Name the parasite shown.
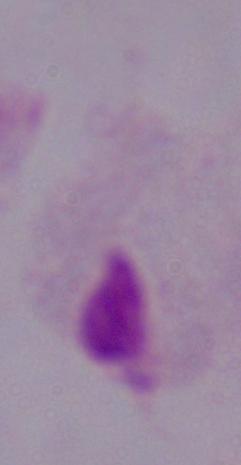
This is a trichomonad.

Photomicrograph. 1000x magnification.